Classify this cell by malaria status.
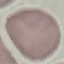
It is uninfected.

Cell patch, automatically extracted from a larger field of view and resized to 64 × 64 pixels. Giemsa stain. Thin blood film. Acquired by smartphone through the microscope eyepiece.